State which parasite is depicted.
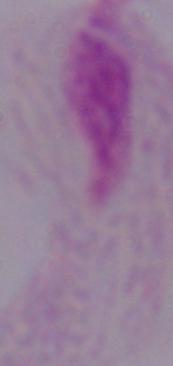

A trichomonad.

Photomicrograph. Captured at 1000x magnification.